Assess this cell for malaria.
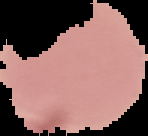
Uninfected.

Summary:
  - Image size: 148×136 pixels
  - Image type: cell region segmented out of the field of view; surrounding area masked to black
  - Preparation: thin blood film